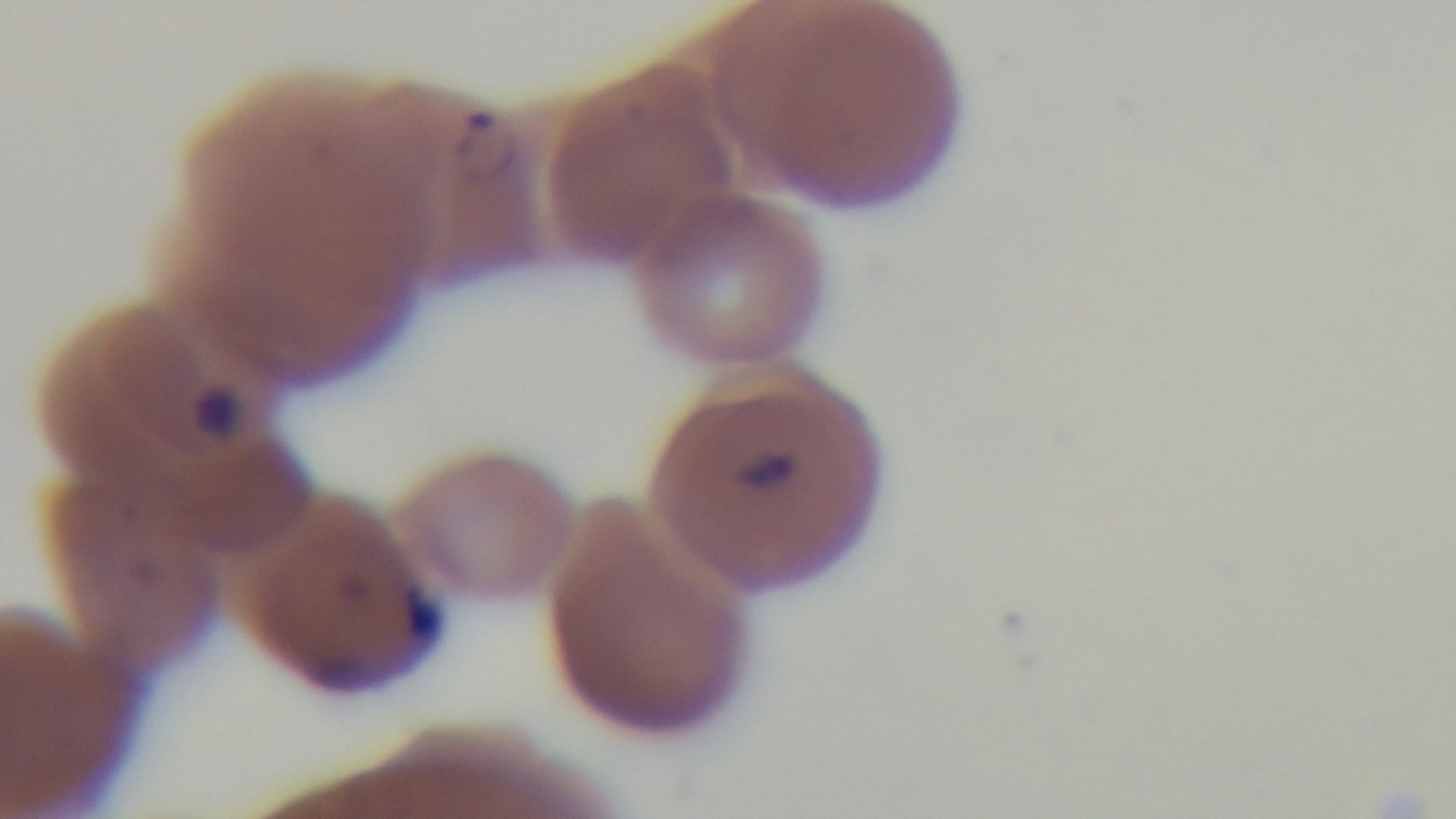

malaria status = infected
stain = Giemsa
field of view = single
preparation = thin
modality = light microscopy
capture = mounted 4K digital camera
objective = 100x oil immersion